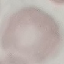
Result: no malaria parasites seen. Automatically extracted cell patch, resized to 64 × 64 pixels. Giemsa stain. Thin blood smear. Acquired by smartphone through the microscope eyepiece.